Identify the parasite.
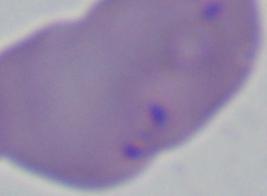
This is Babesia.

Captured at 1000x magnification. Photomicrograph.